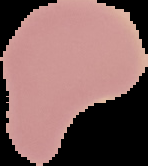
image_type: segmented cell region on a black background
preparation: thin blood film
result: no malaria parasites seen
image_size: 148×166 pixels